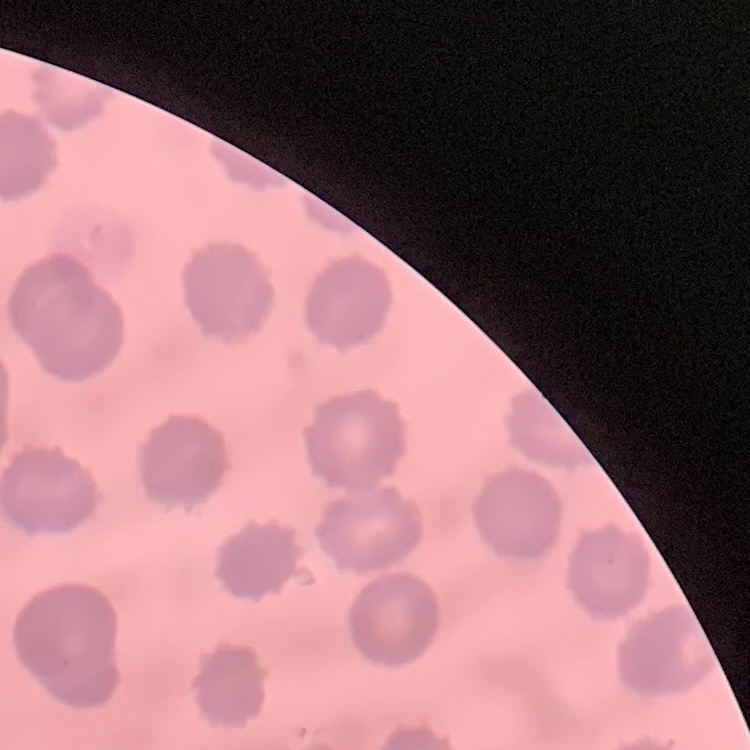 The erythrocytes show no rouleaux formation. Thin peripheral smear. Square crop of a larger photomicrograph. Stained with either Field's or Giemsa.